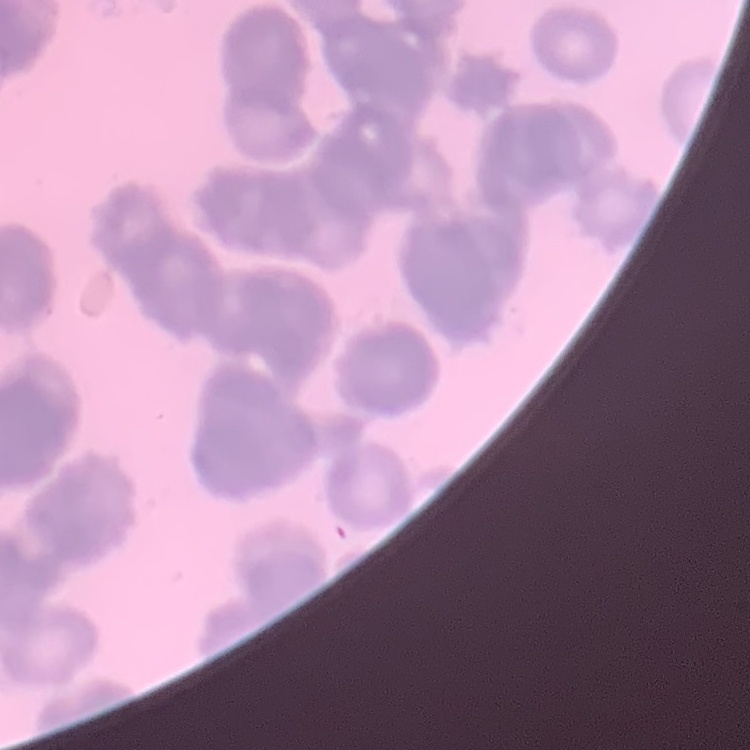

red blood cell morphology = rouleaux formation
preparation = thin blood smear
stain = Field's or Giemsa
image type = one tile cut from a larger photomicrograph